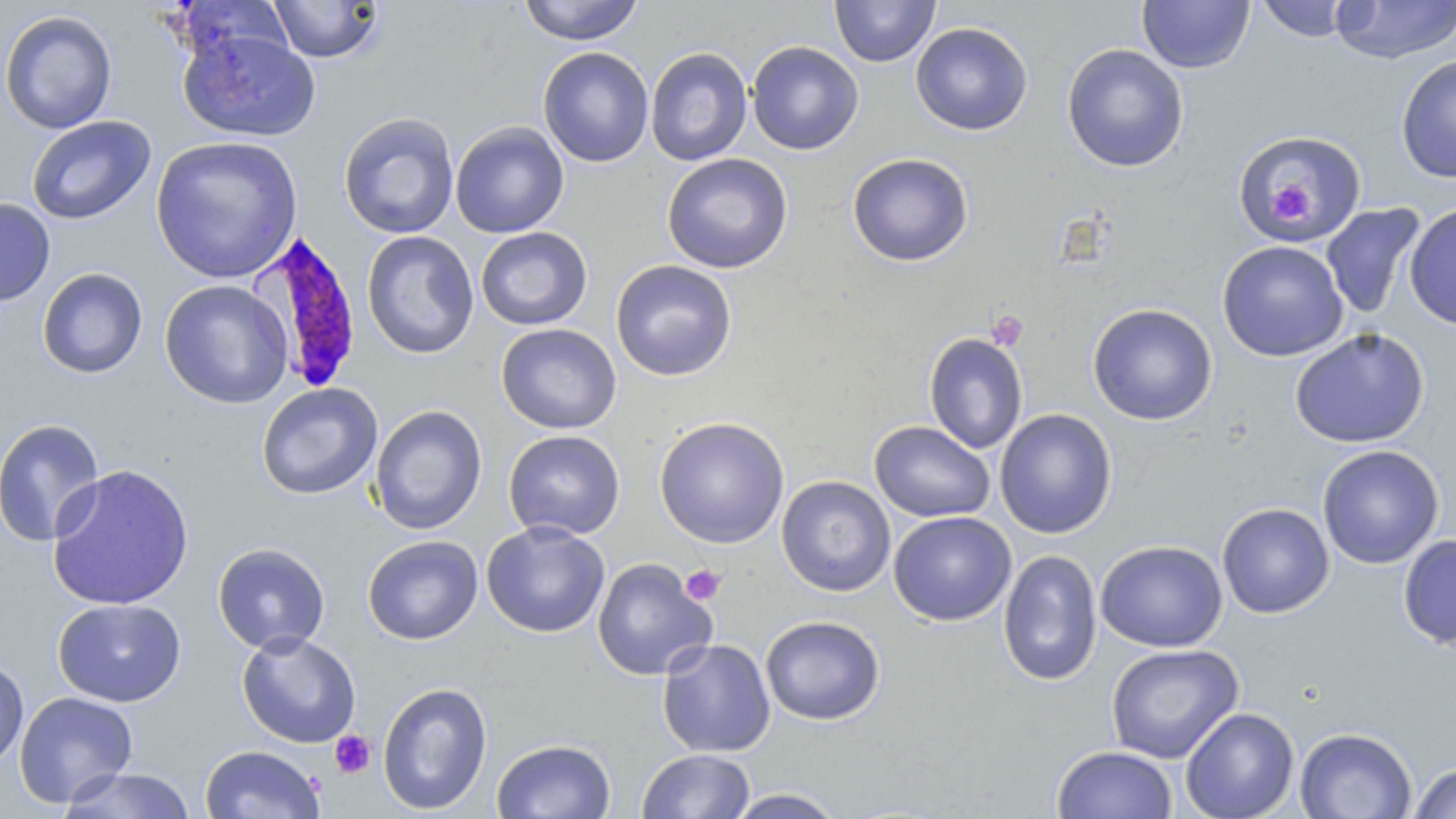

Summary:
  - Coordinate format: approximate bounding boxes as named x1/y1/x2/y2 corners in pixels
  - Platelet locations: (x1=1264, y1=181, x2=1318, y2=226), (x1=986, y1=309, x2=1028, y2=350), (x1=680, y1=564, x2=727, y2=605), (x1=329, y1=731, x2=375, y2=778)
  - Uninfected red blood cell locations: (x1=517, y1=0, x2=645, y2=45), (x1=829, y1=0, x2=941, y2=67), (x1=1253, y1=0, x2=1360, y2=42), (x1=1330, y1=0, x2=1456, y2=64), (x1=266, y1=1, x2=385, y2=64), (x1=1138, y1=1, x2=1255, y2=73), (x1=0, y1=10, x2=118, y2=135), (x1=911, y1=22, x2=1033, y2=136), (x1=178, y1=26, x2=321, y2=142), (x1=746, y1=41, x2=863, y2=155), (x1=1061, y1=44, x2=1189, y2=172), (x1=537, y1=47, x2=653, y2=167), (x1=645, y1=47, x2=752, y2=166), (x1=1395, y1=54, x2=1456, y2=183), (x1=338, y1=112, x2=459, y2=239), (x1=26, y1=115, x2=156, y2=225), (x1=449, y1=121, x2=569, y2=238), (x1=1235, y1=130, x2=1368, y2=245), (x1=150, y1=135, x2=303, y2=284), (x1=662, y1=153, x2=793, y2=274), (x1=847, y1=153, x2=973, y2=267), (x1=0, y1=197, x2=55, y2=306), (x1=1403, y1=201, x2=1456, y2=332), (x1=1320, y1=203, x2=1426, y2=320), (x1=476, y1=227, x2=592, y2=331), (x1=361, y1=231, x2=479, y2=359), (x1=1217, y1=241, x2=1348, y2=362), (x1=610, y1=259, x2=737, y2=381), (x1=37, y1=267, x2=148, y2=379), (x1=159, y1=280, x2=293, y2=409), (x1=1087, y1=303, x2=1218, y2=425), (x1=496, y1=323, x2=622, y2=434), (x1=1290, y1=327, x2=1429, y2=449), (x1=923, y1=332, x2=1028, y2=454), (x1=256, y1=383, x2=382, y2=500), (x1=370, y1=404, x2=487, y2=535), (x1=994, y1=409, x2=1117, y2=539), (x1=654, y1=416, x2=790, y2=548), (x1=0, y1=418, x2=105, y2=548), (x1=869, y1=420, x2=996, y2=523), (x1=503, y1=430, x2=625, y2=540), (x1=1317, y1=445, x2=1443, y2=569), (x1=46, y1=463, x2=195, y2=612), (x1=776, y1=476, x2=896, y2=596), (x1=1216, y1=502, x2=1334, y2=619), (x1=888, y1=510, x2=1016, y2=626), (x1=481, y1=521, x2=610, y2=638), (x1=1397, y1=534, x2=1456, y2=650), (x1=362, y1=535, x2=483, y2=645), (x1=1095, y1=540, x2=1227, y2=652), (x1=212, y1=542, x2=331, y2=654), (x1=998, y1=549, x2=1101, y2=686), (x1=592, y1=557, x2=717, y2=681), (x1=51, y1=598, x2=187, y2=707), (x1=760, y1=615, x2=886, y2=725), (x1=236, y1=631, x2=361, y2=748), (x1=657, y1=638, x2=776, y2=758), (x1=1105, y1=644, x2=1244, y2=763), (x1=0, y1=657, x2=29, y2=770), (x1=377, y1=681, x2=493, y2=815), (x1=13, y1=691, x2=138, y2=808), (x1=1180, y1=707, x2=1299, y2=819), (x1=1294, y1=727, x2=1417, y2=819), (x1=491, y1=738, x2=616, y2=819), (x1=199, y1=745, x2=325, y2=818), (x1=1051, y1=745, x2=1178, y2=819), (x1=636, y1=749, x2=756, y2=819), (x1=1407, y1=762, x2=1456, y2=819), (x1=57, y1=767, x2=197, y2=818), (x1=724, y1=788, x2=846, y2=818)
  - Plasmodium falciparum-infected red blood cell locations: (x1=250, y1=232, x2=362, y2=395)
  - Slide-level diagnosis: Plasmodium falciparum
  - Image size: 1456×819 pixels
  - Stain: May-Grünwald-Giemsa
  - Magnification: 1000x
  - Preparation: thin blood film
  - Field of view: one of a larger specimen
  - Modality: light microscopy